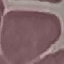

Summary:
  - Malaria status: uninfected
  - Capture: smartphone camera at the microscope eyepiece
  - Stain: Giemsa
  - Image type: cell patch, automatically extracted from a larger field of view and resized to 64 × 64 pixels
  - Preparation: thin blood film